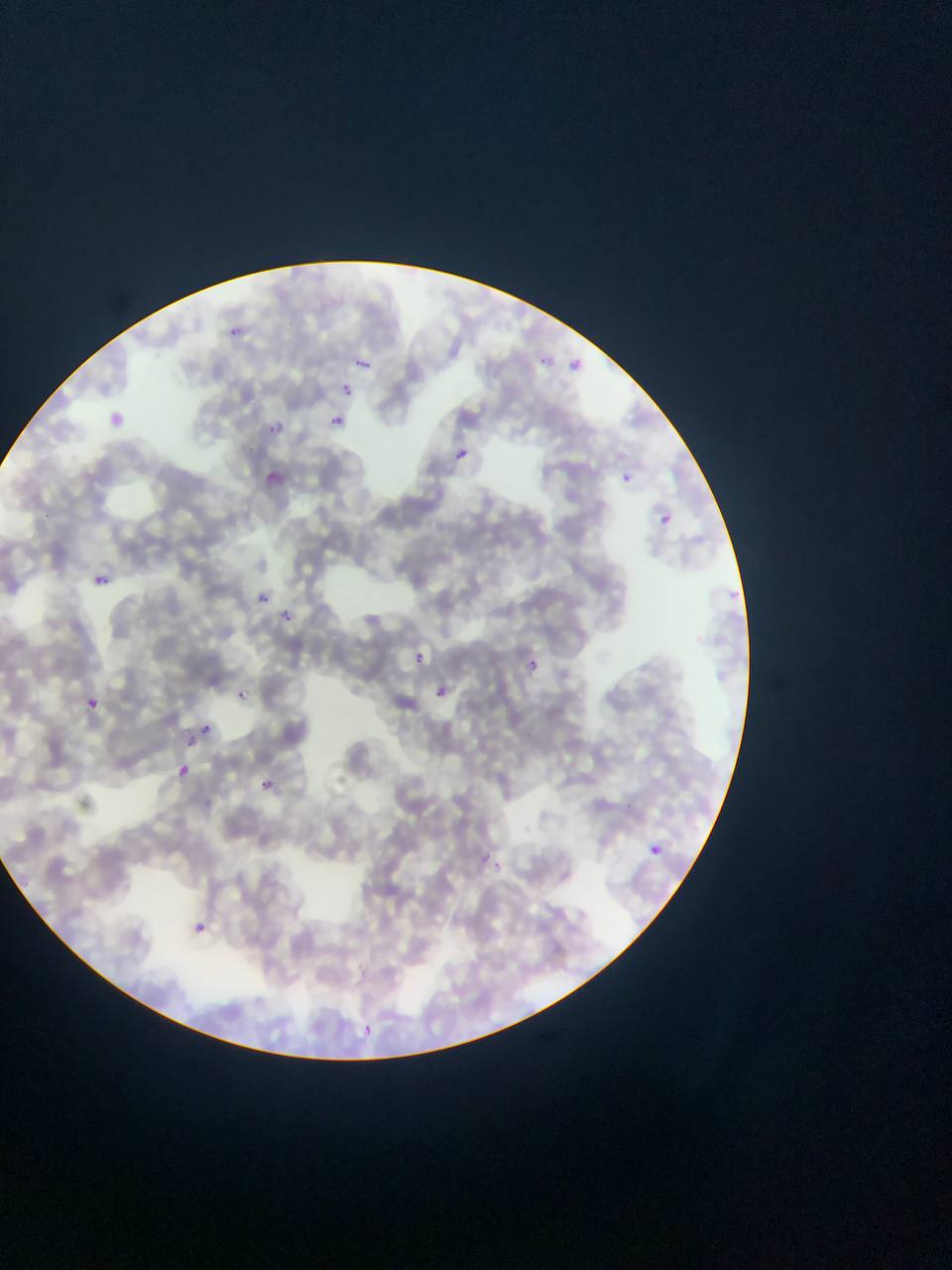

Approximate bounding boxes as left top right bottom in pixels.
Summary:
  - Plasmodium parasite locations: 226 321 250 344; 534 350 555 375; 346 351 382 384; 570 357 590 381; 341 381 356 397; 109 405 143 452; 330 413 347 427; 265 416 290 435; 457 446 470 461; 260 462 289 486; 617 464 648 504; 657 508 678 532; 93 574 110 586; 726 581 747 601; 260 593 270 603; 274 608 292 630; 413 645 444 666; 527 657 541 673; 430 680 453 709; 238 689 248 700; 87 697 97 708; 201 723 212 734; 188 737 197 746; 179 763 193 777; 254 772 287 797; 476 843 512 884; 649 843 662 856; 194 921 215 934; 347 1014 384 1036
  - Image size: 952×1270 pixels
  - Country: Ghana
  - Field of view: single
  - Preparation: thin blood film
  - Capture: mobile-phone photograph through a microscope